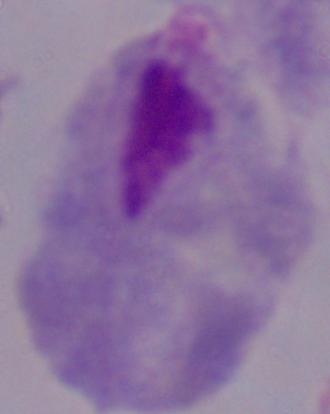
A trichomonad is shown. 1000x magnification. Photomicrograph.